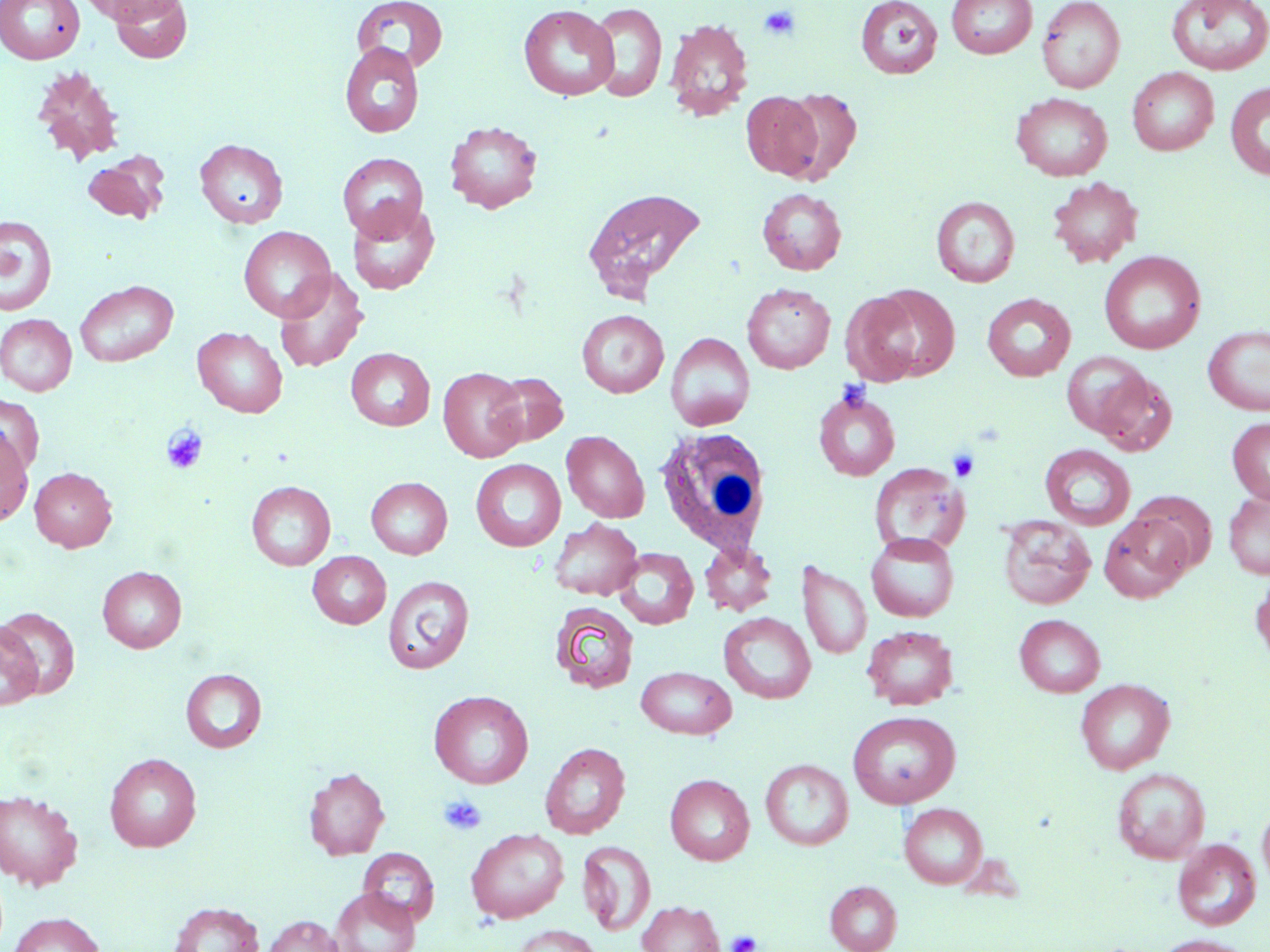
Approximate bounding boxes as (x1,y1)-(x2,y2) corner pairs in pixels. Platelet locations: (758,4)-(801,41), (836,379)-(876,415), (160,424)-(208,475), (948,447)-(981,483), (439,795)-(487,836), (727,930)-(762,952). Uninfected red blood cell locations: (1,0)-(84,64), (78,0)-(185,25), (108,0)-(193,63), (855,0)-(943,79), (946,0)-(1038,59), (1036,0)-(1125,93), (352,1)-(448,74), (1165,1)-(1270,76), (588,3)-(667,102), (518,4)-(619,101), (664,18)-(754,122), (339,42)-(425,138), (31,64)-(126,165), (1127,67)-(1219,155), (1225,81)-(1270,180), (780,87)-(862,182), (741,90)-(825,180), (1011,92)-(1113,181), (444,121)-(543,213), (195,138)-(288,228), (83,152)-(170,224), (338,152)-(428,241), (1047,177)-(1143,268), (580,187)-(708,303), (757,188)-(847,275), (931,196)-(1020,287), (346,202)-(439,294), (0,215)-(57,316), (238,226)-(336,321), (1099,251)-(1205,354), (273,269)-(369,373), (74,280)-(179,367), (741,283)-(835,374), (866,285)-(961,382), (840,291)-(924,386), (982,293)-(1076,382), (577,309)-(668,398), (0,314)-(77,395), (1203,325)-(1270,417), (193,326)-(288,417), (666,332)-(756,431), (346,348)-(435,430), (1060,351)-(1152,438), (438,368)-(527,462), (487,371)-(568,447), (1092,371)-(1178,456), (814,390)-(900,481), (0,393)-(44,476), (1227,417)-(1270,506), (0,427)-(33,527), (561,430)-(649,523), (1039,444)-(1136,530), (471,459)-(566,552), (869,462)-(969,556), (29,466)-(117,552), (365,477)-(452,559), (246,481)-(336,570), (1223,489)-(1270,579), (1129,495)-(1217,575), (1099,512)-(1193,602), (997,514)-(1096,610), (549,518)-(643,601), (866,532)-(959,622), (700,541)-(778,617), (614,547)-(699,630), (308,551)-(391,628), (798,560)-(872,661), (97,566)-(187,652), (1250,571)-(1270,668), (383,575)-(474,674), (549,601)-(639,694), (0,606)-(81,700), (719,612)-(816,703), (1014,614)-(1106,697), (0,621)-(42,710), (862,625)-(959,710), (636,666)-(737,739), (181,669)-(267,753), (1075,678)-(1175,774), (429,690)-(534,789), (847,711)-(960,808), (540,742)-(631,839), (105,753)-(202,851), (760,759)-(853,850), (303,766)-(390,860), (1112,767)-(1210,864), (665,773)-(755,865), (0,789)-(83,891), (899,803)-(988,889), (1258,803)-(1270,892), (466,828)-(569,923), (1172,838)-(1261,930), (577,840)-(657,935), (358,846)-(440,925), (825,880)-(902,952), (330,888)-(420,952), (168,901)-(265,952), (637,901)-(725,952), (8,912)-(105,952), (262,915)-(345,952), (514,924)-(604,952), (1153,935)-(1256,952). White blood cell locations: (653,426)-(774,560). Slide-level diagnosis: no evidence of blood parasites. Thin blood film. May-Grünwald-Giemsa-stained preparation. One field of a larger specimen. 1000x magnification. Light microscopy. Image is 1270×952 pixels.